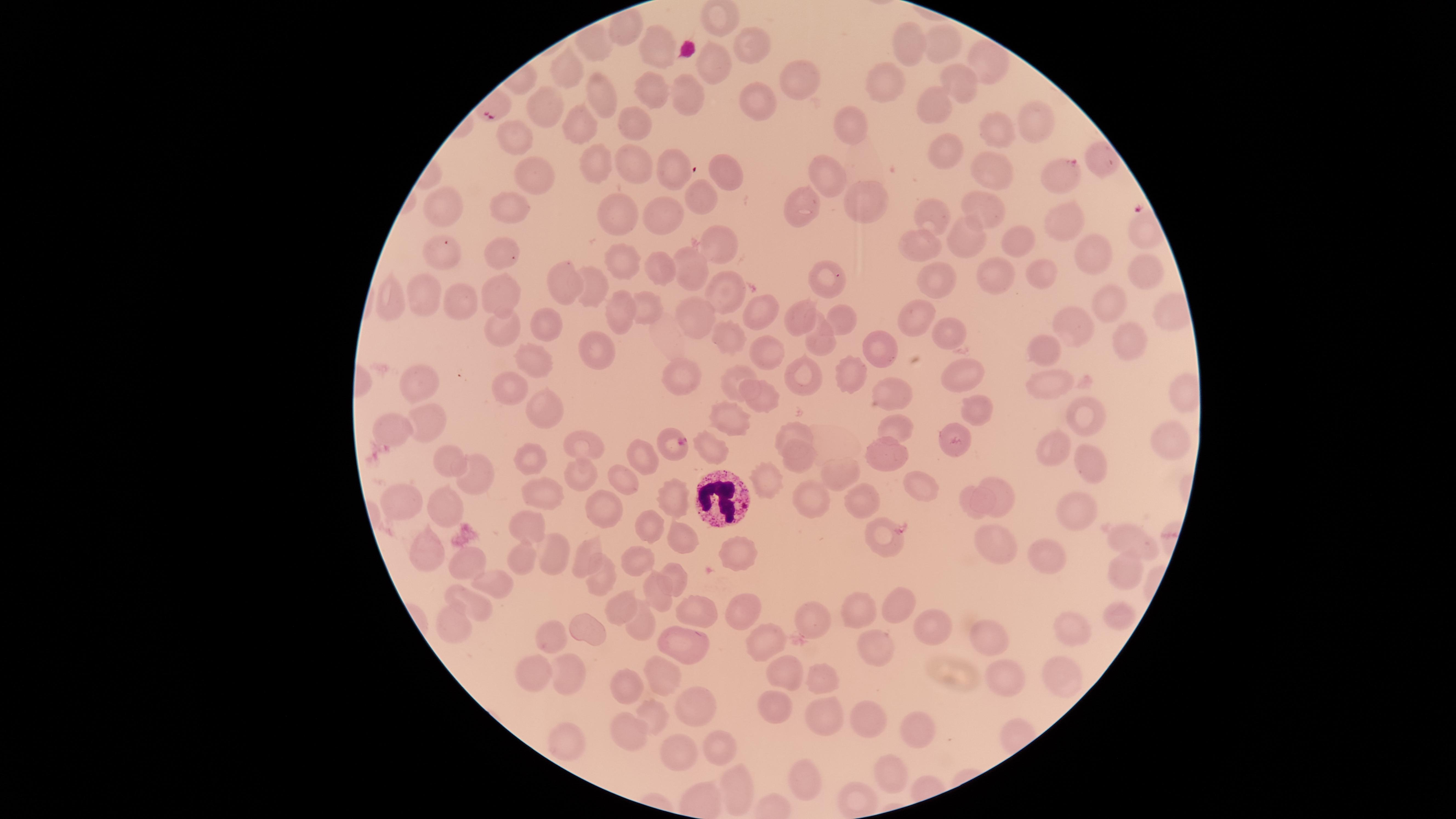

Approximate marker points, in pixels from the top-left corner.
Summary:
  - Parasitized red blood cells: (x=1063, y=172), (x=670, y=443)
  - White blood cells: (x=720, y=497)
  - Uninfected red blood cells: (x=620, y=23), (x=592, y=46), (x=655, y=46), (x=747, y=46), (x=908, y=46), (x=942, y=50), (x=714, y=60), (x=990, y=63), (x=565, y=68), (x=802, y=78), (x=959, y=79), (x=888, y=80), (x=602, y=85), (x=643, y=90), (x=681, y=93), (x=753, y=97), (x=935, y=104), (x=542, y=110), (x=1038, y=116), (x=632, y=121), (x=585, y=123), (x=994, y=130), (x=849, y=131), (x=520, y=139), (x=948, y=151), (x=632, y=158), (x=1098, y=160), (x=594, y=162), (x=676, y=167), (x=534, y=169), (x=722, y=171), (x=997, y=171), (x=823, y=178), (x=701, y=196), (x=512, y=203), (x=986, y=203), (x=864, y=204), (x=445, y=207), (x=664, y=211), (x=804, y=211), (x=934, y=211), (x=621, y=212), (x=1057, y=222), (x=1026, y=236), (x=964, y=238), (x=723, y=244), (x=922, y=244), (x=503, y=245), (x=1094, y=251), (x=445, y=259), (x=622, y=262), (x=659, y=265), (x=1138, y=265), (x=686, y=266), (x=996, y=274), (x=1041, y=275), (x=937, y=276), (x=568, y=284), (x=831, y=286), (x=592, y=287), (x=493, y=288), (x=728, y=292), (x=428, y=296), (x=466, y=302), (x=391, y=303), (x=645, y=307), (x=1113, y=307), (x=756, y=310), (x=701, y=312), (x=801, y=315), (x=917, y=316), (x=618, y=317), (x=844, y=317), (x=1079, y=325), (x=547, y=326), (x=499, y=328), (x=954, y=330), (x=726, y=333), (x=1131, y=337), (x=823, y=338), (x=884, y=341), (x=1045, y=346), (x=766, y=347), (x=587, y=348), (x=537, y=364), (x=427, y=373), (x=803, y=373), (x=962, y=374), (x=1050, y=377), (x=852, y=378), (x=683, y=379), (x=733, y=379), (x=886, y=390), (x=509, y=391), (x=760, y=392), (x=546, y=406), (x=727, y=414), (x=980, y=414), (x=1088, y=415), (x=898, y=424), (x=430, y=425), (x=388, y=429), (x=794, y=432), (x=1171, y=439), (x=956, y=442), (x=1056, y=444), (x=710, y=448), (x=585, y=449), (x=886, y=453), (x=447, y=457), (x=795, y=457), (x=638, y=460), (x=530, y=462), (x=1091, y=462), (x=477, y=470), (x=839, y=471), (x=578, y=473), (x=768, y=477), (x=619, y=478), (x=917, y=485), (x=969, y=496), (x=815, y=497), (x=1004, y=497), (x=401, y=498), (x=541, y=498), (x=671, y=499), (x=865, y=500), (x=603, y=504), (x=440, y=508), (x=1065, y=511), (x=527, y=524), (x=654, y=526), (x=882, y=536), (x=1124, y=539), (x=676, y=540), (x=420, y=546), (x=996, y=547), (x=525, y=553), (x=548, y=553), (x=740, y=556), (x=462, y=557), (x=590, y=557), (x=639, y=560), (x=1051, y=560), (x=1120, y=570), (x=492, y=581), (x=597, y=581), (x=673, y=583), (x=654, y=590), (x=475, y=604), (x=738, y=604), (x=620, y=606), (x=695, y=607), (x=897, y=608), (x=855, y=611), (x=1120, y=614), (x=818, y=618), (x=450, y=622), (x=642, y=624), (x=1067, y=626), (x=936, y=627), (x=587, y=634), (x=996, y=634), (x=557, y=635), (x=685, y=637), (x=761, y=644), (x=880, y=652), (x=530, y=668), (x=1056, y=669), (x=564, y=672), (x=664, y=672), (x=782, y=674), (x=1002, y=679), (x=817, y=682), (x=628, y=686), (x=778, y=708), (x=823, y=708), (x=659, y=710), (x=869, y=714), (x=694, y=717), (x=917, y=730), (x=628, y=733), (x=565, y=741), (x=725, y=750), (x=678, y=755), (x=888, y=768), (x=809, y=771), (x=738, y=790), (x=857, y=797)
  - Presence: malaria parasites seen
  - Field of view: single
  - Stain: Giemsa
  - Capture: smartphone photograph through the microscope eyepiece
  - Species: Plasmodium falciparum
  - Image size: 1456×819 pixels
  - Visible region: circular
  - Preparation: thin blood film